State the blood parasite species.
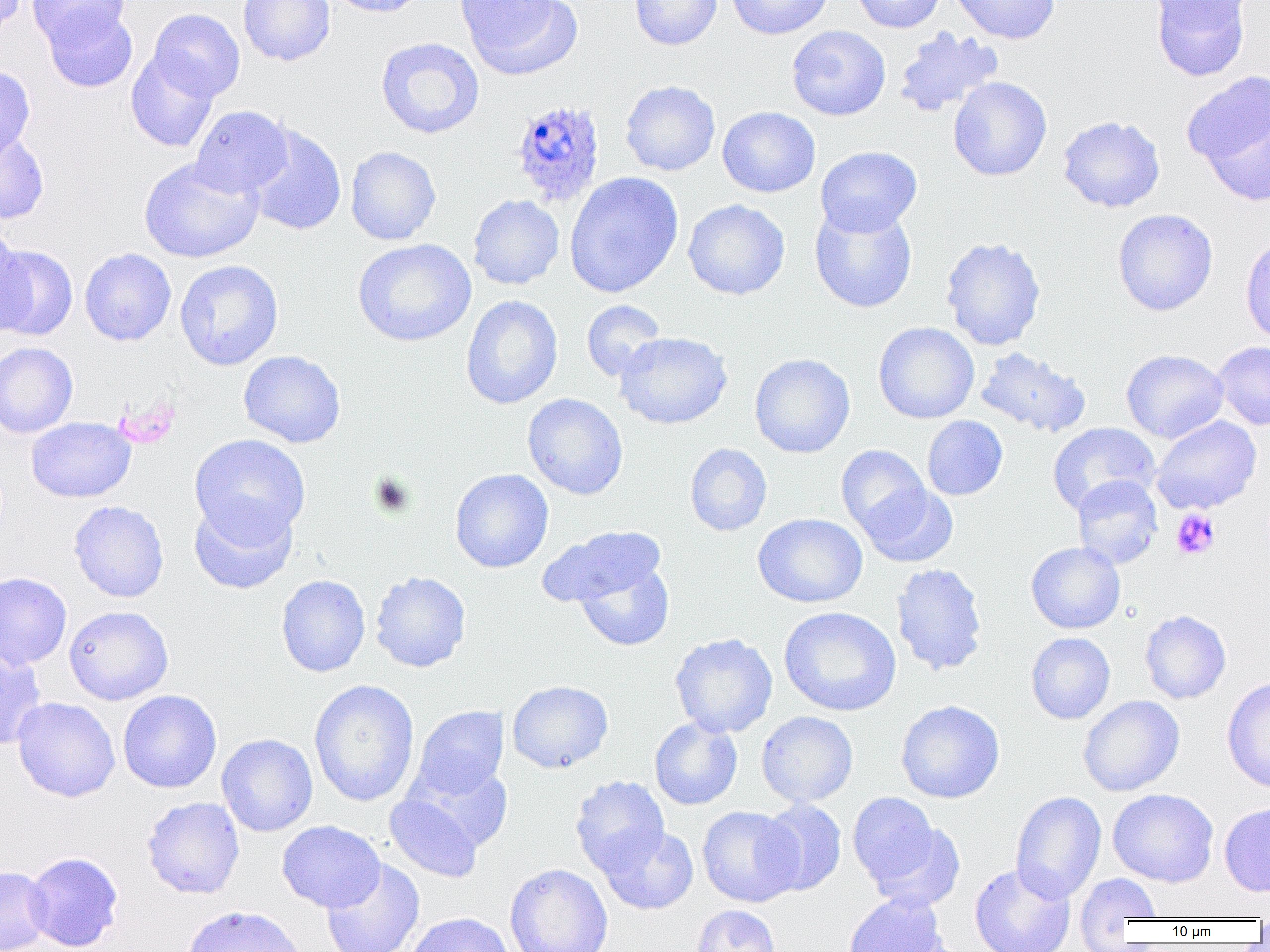

Plasmodium ovale.

field of view = one of a larger specimen
Plasmodium ovale-infected red blood cell locations = approximate bounding boxes as (x1, y1, x2, y2) in pixels: (515, 98, 608, 206)
modality = light microscopy
preparation = thin blood film
platelet locations = approximate bounding boxes as (x1, y1, x2, y2) in pixels: (371, 472, 415, 516), (1171, 508, 1220, 560)
image size = 1270×952 pixels
magnification = 1000x
uninfected red blood cell locations = approximate bounding boxes as (x1, y1, x2, y2) in pixels: (0, 0, 26, 37), (27, 0, 130, 51), (238, 0, 336, 66), (327, 0, 429, 18), (457, 0, 580, 78), (629, 0, 722, 50), (726, 0, 833, 39), (849, 0, 946, 33), (949, 0, 1060, 44), (1149, 0, 1257, 25), (1151, 0, 1251, 81), (43, 6, 138, 93), (148, 8, 245, 102), (786, 25, 890, 120), (893, 27, 1004, 118), (376, 36, 485, 139), (126, 50, 220, 152), (0, 65, 35, 161), (1183, 70, 1270, 194), (948, 77, 1052, 181), (620, 80, 721, 176), (191, 105, 293, 198), (717, 106, 821, 198), (1058, 115, 1166, 213), (246, 125, 346, 236), (0, 127, 49, 224), (815, 145, 922, 236), (345, 146, 441, 245), (138, 156, 264, 263), (564, 171, 684, 298), (468, 194, 564, 290), (683, 199, 790, 300), (809, 202, 918, 314), (1112, 208, 1218, 316), (0, 229, 34, 338), (1240, 232, 1270, 347), (940, 237, 1046, 351), (353, 239, 476, 346), (1, 245, 78, 341), (79, 248, 176, 346), (174, 259, 284, 370), (461, 295, 563, 409), (581, 300, 667, 381), (873, 322, 980, 423), (614, 331, 732, 430), (1212, 341, 1270, 431), (0, 342, 78, 438), (975, 346, 1092, 438), (1121, 349, 1229, 443), (238, 350, 346, 448), (749, 353, 855, 458), (522, 393, 628, 500), (922, 416, 1008, 500), (1151, 416, 1261, 514), (26, 417, 136, 502), (1047, 422, 1161, 515), (190, 434, 310, 544), (685, 443, 772, 536), (836, 444, 930, 537), (450, 469, 553, 573), (1072, 475, 1163, 569), (858, 484, 959, 568), (189, 498, 298, 594), (69, 500, 169, 602), (753, 512, 868, 608), (536, 525, 666, 610), (1026, 542, 1125, 634), (573, 557, 675, 652), (891, 563, 988, 676), (370, 571, 471, 672), (0, 572, 72, 670), (276, 574, 370, 677), (64, 605, 174, 705), (779, 606, 901, 716), (1140, 610, 1231, 704), (1026, 632, 1116, 724), (670, 633, 778, 738), (0, 648, 46, 750), (1222, 677, 1270, 794), (309, 679, 420, 807), (507, 680, 613, 773), (118, 689, 222, 793), (1078, 695, 1184, 797), (12, 697, 120, 802), (896, 700, 1005, 804), (411, 705, 508, 800), (756, 711, 858, 807), (649, 717, 742, 810), (216, 733, 318, 837), (404, 759, 514, 852), (570, 776, 670, 876), (1107, 788, 1219, 888), (1010, 791, 1106, 904), (848, 792, 946, 893), (385, 794, 483, 882), (142, 796, 245, 899), (757, 799, 847, 895), (1219, 802, 1270, 897), (697, 805, 803, 907), (277, 820, 385, 912), (865, 821, 966, 914), (598, 825, 698, 915), (24, 852, 123, 952), (321, 859, 425, 952), (505, 862, 613, 952), (970, 862, 1076, 952), (0, 866, 53, 952), (1075, 873, 1161, 943), (843, 892, 949, 952), (182, 904, 307, 952), (690, 905, 781, 952), (404, 912, 514, 952), (1254, 912, 1270, 940)